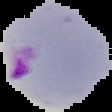
Summary:
  - Result: malaria parasites identified
  - Preparation: thin blood film
  - Image size: 112×112 pixels
  - Image type: segmented cell region on a black background